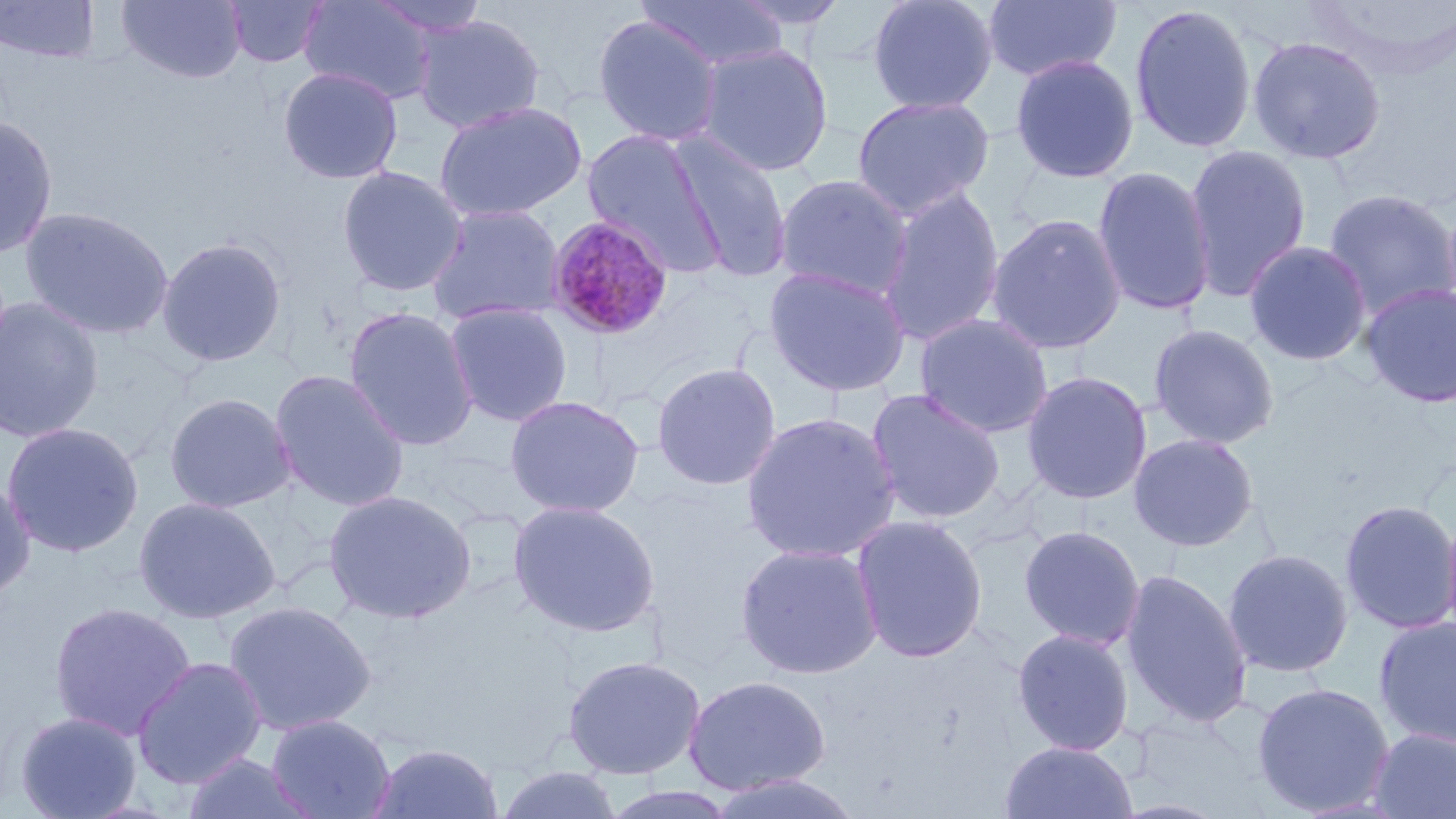
Approximate bounding boxes as (x1,y1)-(x2,y2) corner pairs in pixels. Plasmodium malariae-infected red blood cell locations: (544,214)-(676,340). Uninfected red blood cell locations: (1,0)-(102,64), (117,0)-(247,84), (224,0)-(329,68), (298,0)-(437,105), (366,0)-(495,39), (636,0)-(788,71), (729,0)-(851,30), (867,0)-(999,116), (981,0)-(1121,83), (1301,1)-(1456,79), (1128,3)-(1258,154), (412,13)-(546,134), (592,14)-(724,146), (1247,35)-(1387,165), (695,42)-(834,177), (1009,54)-(1140,184), (277,65)-(403,185), (851,95)-(995,220), (433,100)-(588,223), (0,115)-(59,259), (580,128)-(728,276), (670,135)-(793,283), (1183,143)-(1312,302), (336,165)-(468,297), (1092,165)-(1217,317), (773,173)-(914,301), (876,185)-(1006,348), (1322,188)-(1456,321), (425,203)-(566,327), (19,206)-(174,340), (985,213)-(1127,355), (156,236)-(287,367), (1244,240)-(1372,366), (763,264)-(912,397), (1359,281)-(1456,408), (0,296)-(105,443), (443,302)-(573,427), (344,305)-(479,452), (913,313)-(1055,438), (1147,323)-(1281,450), (651,362)-(781,491), (269,369)-(411,512), (1021,371)-(1152,505), (865,388)-(1006,525), (163,392)-(297,514), (505,395)-(645,518), (740,411)-(902,564), (1,421)-(144,558), (1128,432)-(1260,552), (0,477)-(36,602), (324,489)-(477,624), (133,495)-(281,624), (508,499)-(660,637), (1338,499)-(1456,635), (1440,505)-(1456,650), (851,515)-(988,663), (1018,525)-(1145,650), (734,541)-(884,679), (1221,547)-(1354,678), (1119,568)-(1253,730), (222,600)-(377,737), (48,601)-(196,740), (1373,616)-(1456,749), (1011,628)-(1134,756), (562,654)-(706,780), (131,655)-(268,789), (683,675)-(831,795), (1251,682)-(1395,816), (14,710)-(143,819), (266,713)-(396,819), (1367,727)-(1456,819), (998,741)-(1138,818), (366,742)-(505,819), (180,752)-(317,819), (492,766)-(625,819), (703,772)-(865,819), (599,786)-(742,819). Slide-level diagnosis: Plasmodium malariae. Light microscopy. Image is 1456×819 pixels. Thin blood film. May-Grünwald-Giemsa-stained preparation. Single field of view. 1000x magnification.